Identify the parasite.
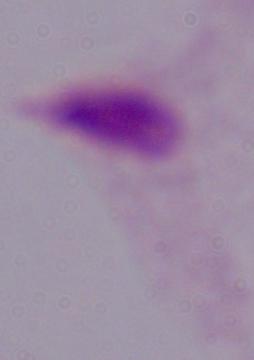
This is a trichomonad.

Summary:
  - Modality: micrograph
  - Magnification: 1000x